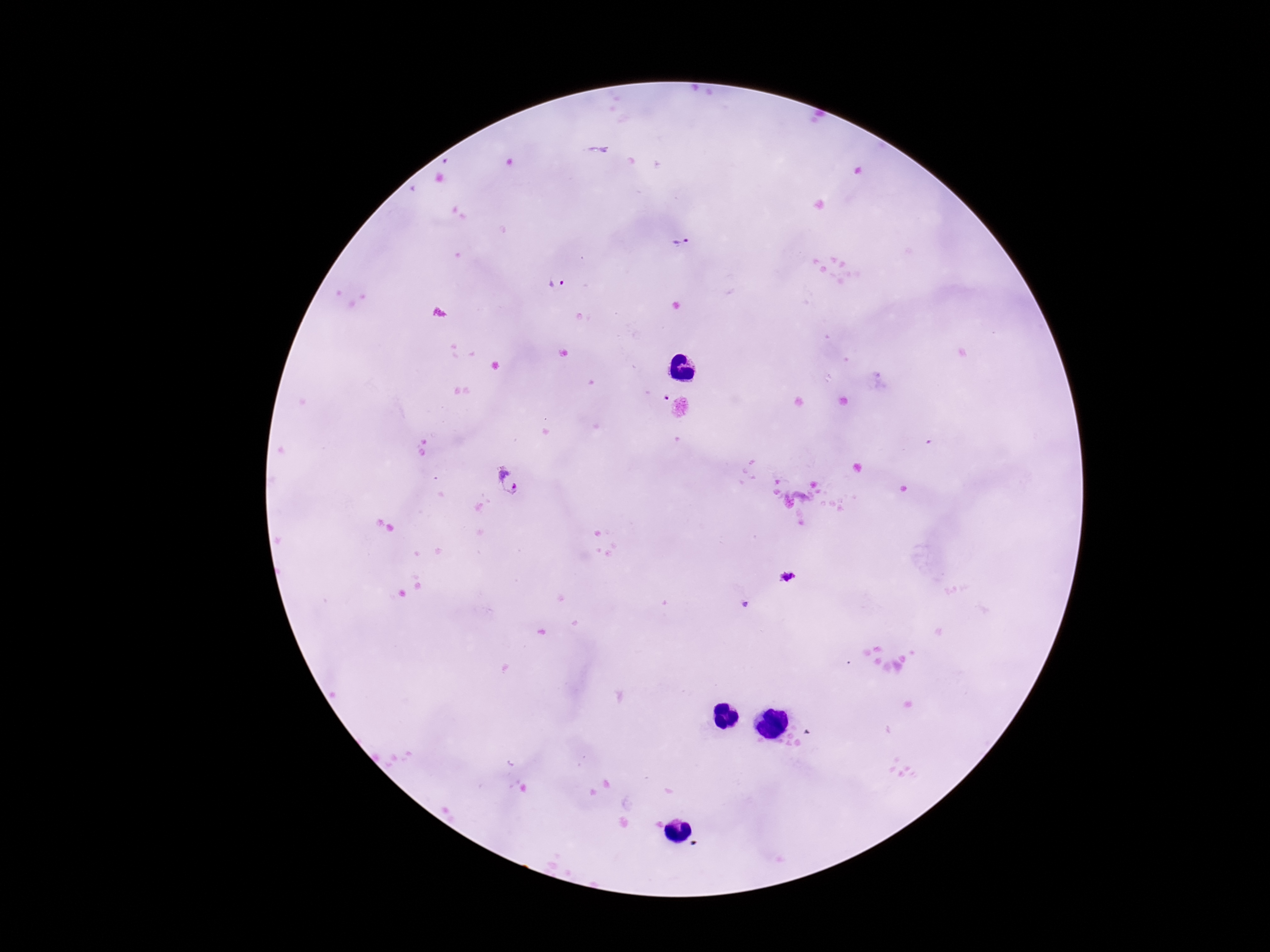

field_of_view: one from this slide
preparation: thick peripheral-blood smear
stain: Giemsa
patient_malaria_status: infected
magnification: 100x
image_size: 1270×952 pixels
plasmodium_parasite_locations: 'approximate centers as [x, y] in pixels: [681, 242], [556, 284], [511, 483], [788, 577], [746, 604]'
capture: smartphone camera through the microscope eyepiece